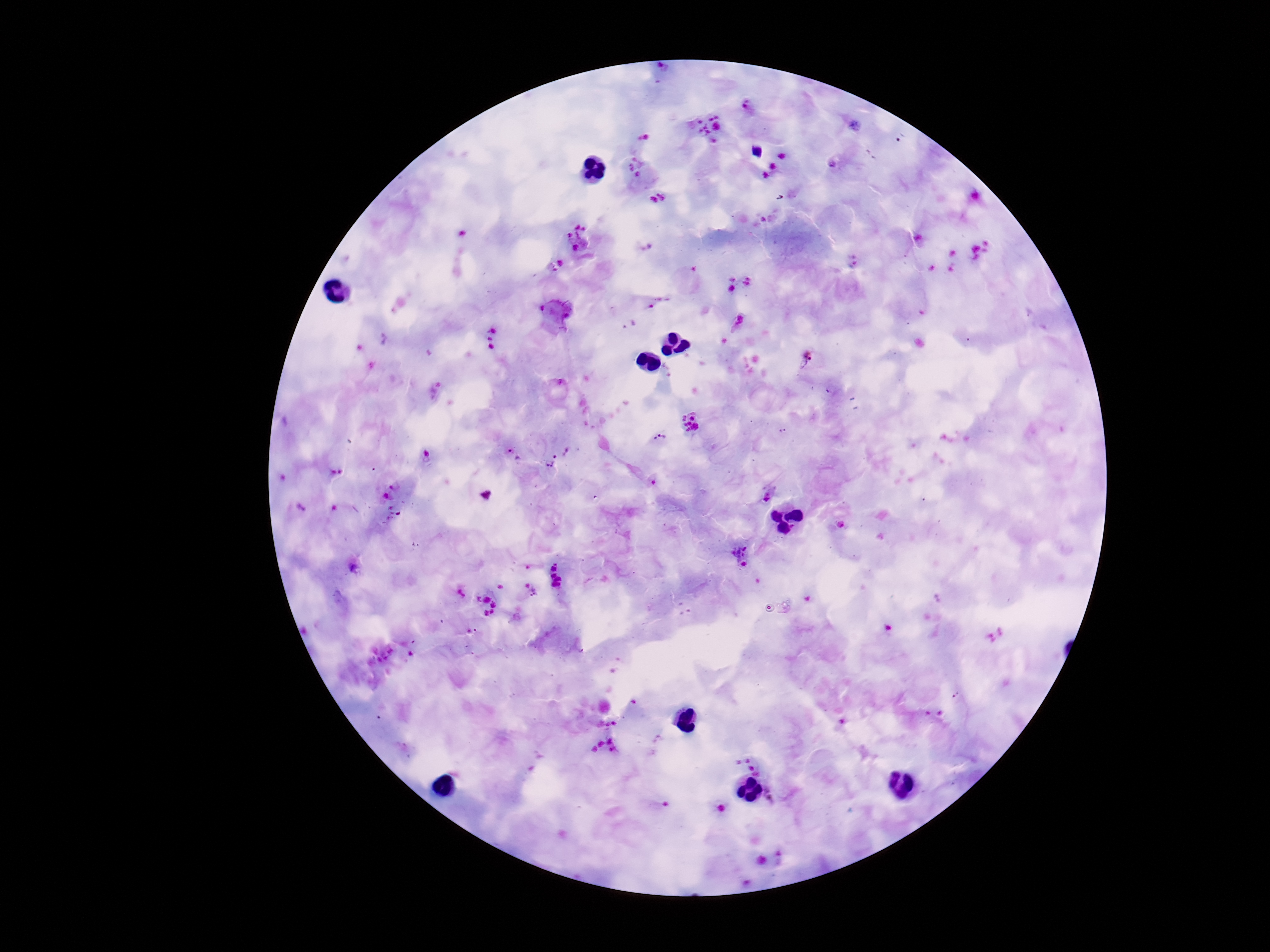

{
  "field_of_view": "one from this slide",
  "stain": "Giemsa",
  "image_size": "1270×952 pixels",
  "plasmodium_parasite_locations": "approximate centers as (x, y) in pixels: (748, 108), (708, 128), (643, 136), (782, 156), (635, 166), (772, 167), (766, 177), (665, 194), (653, 201), (579, 238), (740, 322), (495, 328), (491, 343), (809, 358), (557, 389), (689, 424), (782, 429), (660, 439), (566, 450), (509, 451), (550, 462), (655, 484), (392, 486), (769, 493), (487, 494), (386, 496), (299, 507), (556, 562), (744, 565), (554, 569), (554, 575), (558, 579), (555, 586), (534, 593), (478, 598), (486, 599), (493, 605), (493, 613), (484, 614), (958, 695)",
  "preparation": "thick peripheral-blood smear",
  "capture": "smartphone camera through the microscope eyepiece",
  "magnification": "100x",
  "patient_malaria_status": "positive"
}